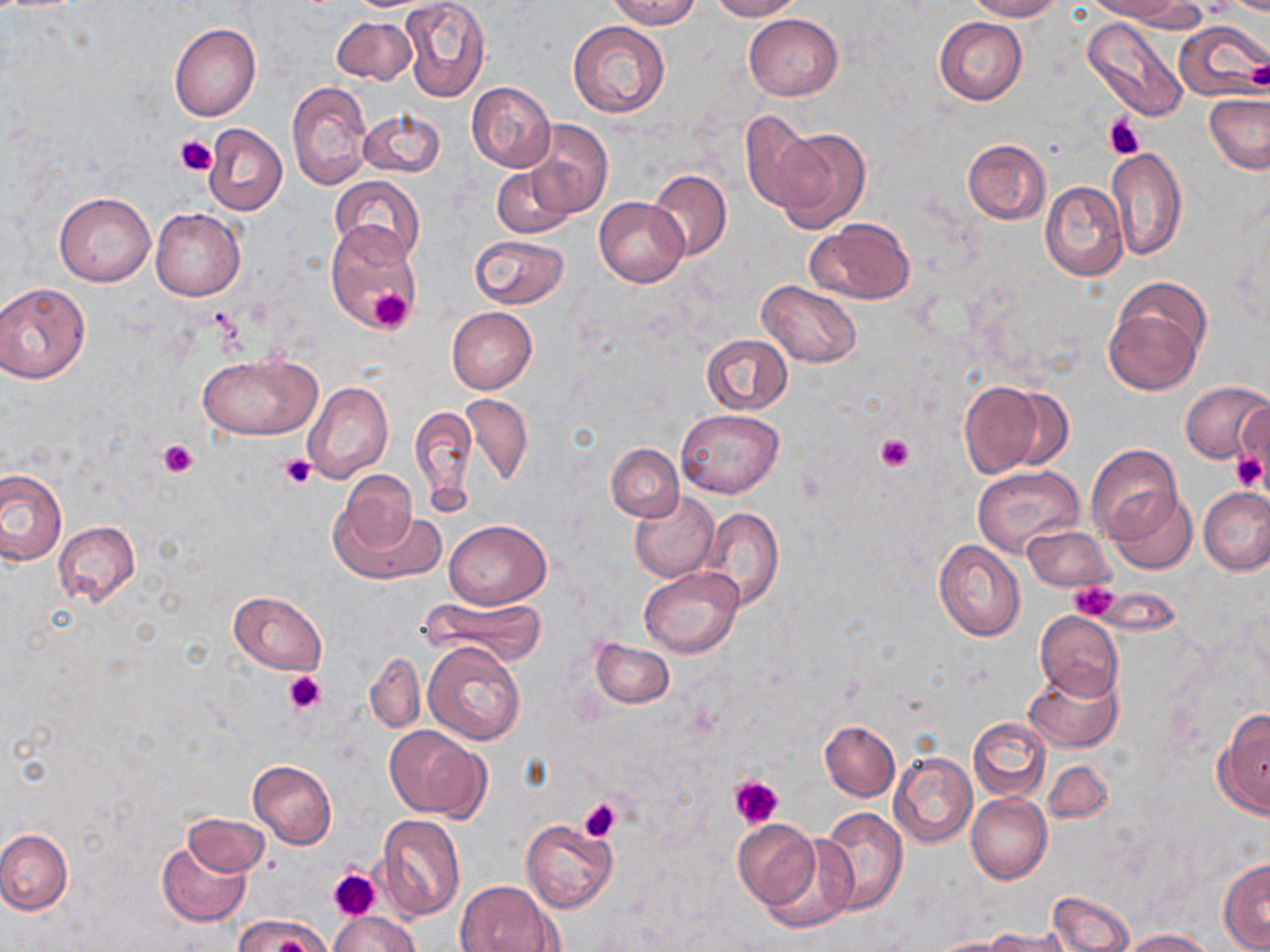

Summary:
  - Coordinate format: approximate bounding boxes as (x1, y1, x2, y2) in pixels
  - Platelet locations: (1198, 0, 1238, 15), (1244, 61, 1270, 91), (1103, 115, 1145, 159), (175, 134, 215, 173), (369, 291, 414, 332), (874, 432, 916, 472), (159, 438, 200, 477), (1231, 451, 1267, 492), (279, 454, 315, 488), (1071, 580, 1120, 622), (283, 670, 329, 715), (729, 774, 784, 829), (578, 799, 622, 841), (329, 868, 378, 920)
  - Uninfected red blood cell locations: (401, 0, 489, 102), (605, 0, 701, 29), (708, 0, 803, 20), (965, 0, 1062, 20), (1087, 0, 1188, 22), (743, 14, 843, 101), (934, 16, 1027, 104), (331, 17, 418, 85), (1082, 17, 1189, 121), (567, 20, 671, 119), (169, 22, 262, 122), (1175, 22, 1266, 99), (287, 79, 371, 191), (467, 82, 555, 172), (1204, 94, 1270, 174), (356, 107, 444, 179), (741, 110, 823, 214), (523, 119, 613, 219), (203, 123, 287, 215), (767, 127, 871, 235), (962, 139, 1050, 224), (1107, 147, 1186, 261), (492, 166, 573, 239), (646, 168, 732, 260), (331, 177, 424, 261), (1040, 181, 1128, 281), (54, 192, 154, 286), (595, 198, 687, 287), (151, 208, 245, 300), (808, 216, 916, 305), (324, 224, 418, 329), (469, 234, 568, 309), (1104, 278, 1211, 396), (756, 280, 862, 368), (0, 281, 91, 384), (447, 306, 537, 393), (701, 334, 793, 414), (200, 353, 322, 438), (304, 381, 393, 483), (960, 381, 1044, 479), (1180, 381, 1270, 464), (999, 388, 1076, 471), (461, 392, 533, 486), (1233, 404, 1269, 478), (411, 405, 477, 508), (676, 409, 783, 499), (607, 443, 683, 520), (1086, 445, 1182, 546), (972, 466, 1082, 559), (0, 468, 66, 564), (333, 469, 420, 562), (1198, 487, 1270, 575), (1108, 490, 1197, 575), (629, 492, 720, 582), (334, 499, 446, 585), (699, 508, 783, 610), (444, 519, 550, 608), (52, 521, 141, 609), (1023, 524, 1113, 592), (934, 540, 1026, 641), (639, 566, 742, 657), (229, 590, 326, 674), (419, 595, 546, 666), (1035, 611, 1123, 698), (590, 638, 674, 708), (422, 640, 525, 745), (367, 652, 425, 732), (1025, 665, 1124, 753), (1215, 710, 1270, 818), (969, 717, 1050, 799), (821, 721, 900, 801), (385, 724, 489, 820), (888, 751, 977, 848), (248, 759, 336, 848), (1043, 762, 1112, 823), (966, 793, 1051, 884), (816, 807, 907, 915), (183, 813, 270, 876), (376, 814, 466, 923), (520, 818, 617, 915), (732, 818, 820, 910), (0, 828, 72, 915), (759, 831, 857, 931), (157, 840, 251, 928), (1218, 858, 1270, 951), (457, 880, 560, 951), (1048, 889, 1134, 952), (328, 912, 421, 952), (234, 914, 331, 952), (987, 927, 1070, 952), (1120, 929, 1216, 951), (930, 938, 1016, 952)
  - Slide-level diagnosis: no evidence of blood parasites
  - Preparation: thin blood smear
  - Modality: light microscopy
  - Image size: 1270×952 pixels
  - Stain: May-Grünwald-Giemsa
  - Field of view: one of a larger specimen
  - Magnification: 1000x